Outline each blood parasite and name the species.
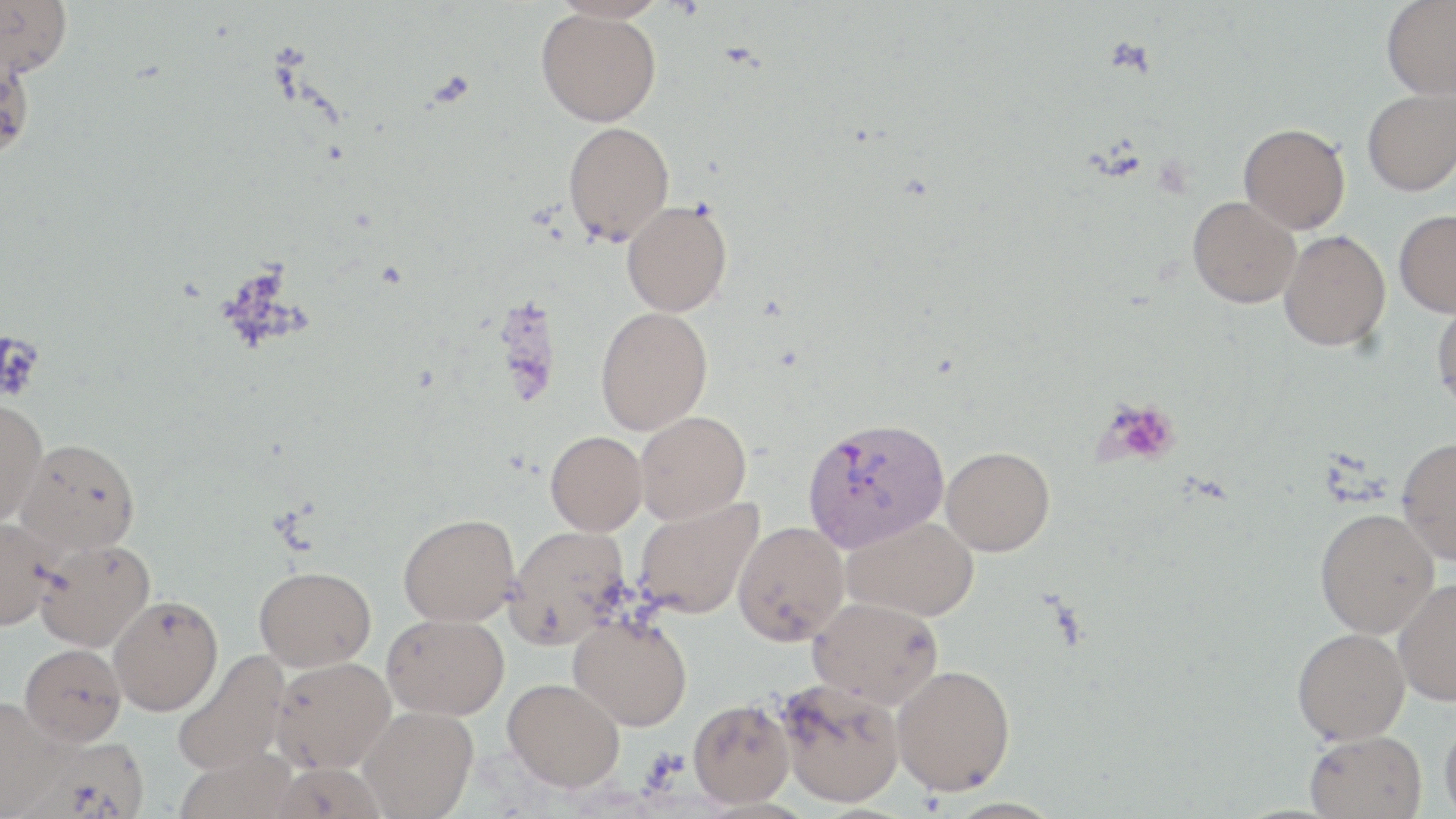

Approximate bounding boxes as (x1,y1)-(x2,y2) corner pairs in pixels.
Plasmodium vivax-infected red blood cells: (802,416)-(949,553).
No Plasmodium falciparum, Plasmodium ovale, Plasmodium malariae, Babesia divergens, or Trypanosoma brucei observed.

slide-level diagnosis = Plasmodium vivax
image size = 1456×819 pixels
modality = light microscopy
field of view = single
uninfected red blood cell locations = approximate bounding boxes as (x1,y1)-(x2,y2) corner pairs in pixels: (0,0)-(73,79), (1381,0)-(1456,99), (536,8)-(661,126), (0,51)-(35,161), (1362,88)-(1456,196), (563,121)-(675,245), (1238,123)-(1350,234), (1187,196)-(1300,308), (621,200)-(732,316), (1394,209)-(1456,317), (1279,231)-(1391,352), (1431,300)-(1456,415), (595,306)-(713,435), (0,397)-(47,526), (635,411)-(751,523), (545,431)-(647,535), (1396,437)-(1456,564), (16,438)-(140,555), (941,446)-(1055,556), (634,497)-(763,620), (1315,508)-(1439,638), (398,513)-(520,627), (843,515)-(978,621), (0,516)-(58,631), (733,520)-(849,646), (505,525)-(630,649), (34,538)-(155,652), (254,565)-(376,670), (1392,578)-(1456,706), (108,595)-(223,716), (807,595)-(943,708), (382,613)-(509,720), (569,613)-(692,731), (1292,627)-(1410,744), (19,643)-(126,746), (172,649)-(291,775), (270,656)-(396,774), (891,664)-(1016,795), (503,678)-(625,791), (775,678)-(905,808), (0,696)-(67,818), (688,698)-(794,807), (359,705)-(478,818), (1439,711)-(1456,818), (1304,730)-(1427,819), (23,735)-(149,818)
preparation = thin blood smear
magnification = 1000x
platelet locations = approximate bounding boxes as (x1,y1)-(x2,y2) corner pairs in pixels: (0,331)-(45,401), (1100,400)-(1181,466)
stain = May-Grünwald-Giemsa